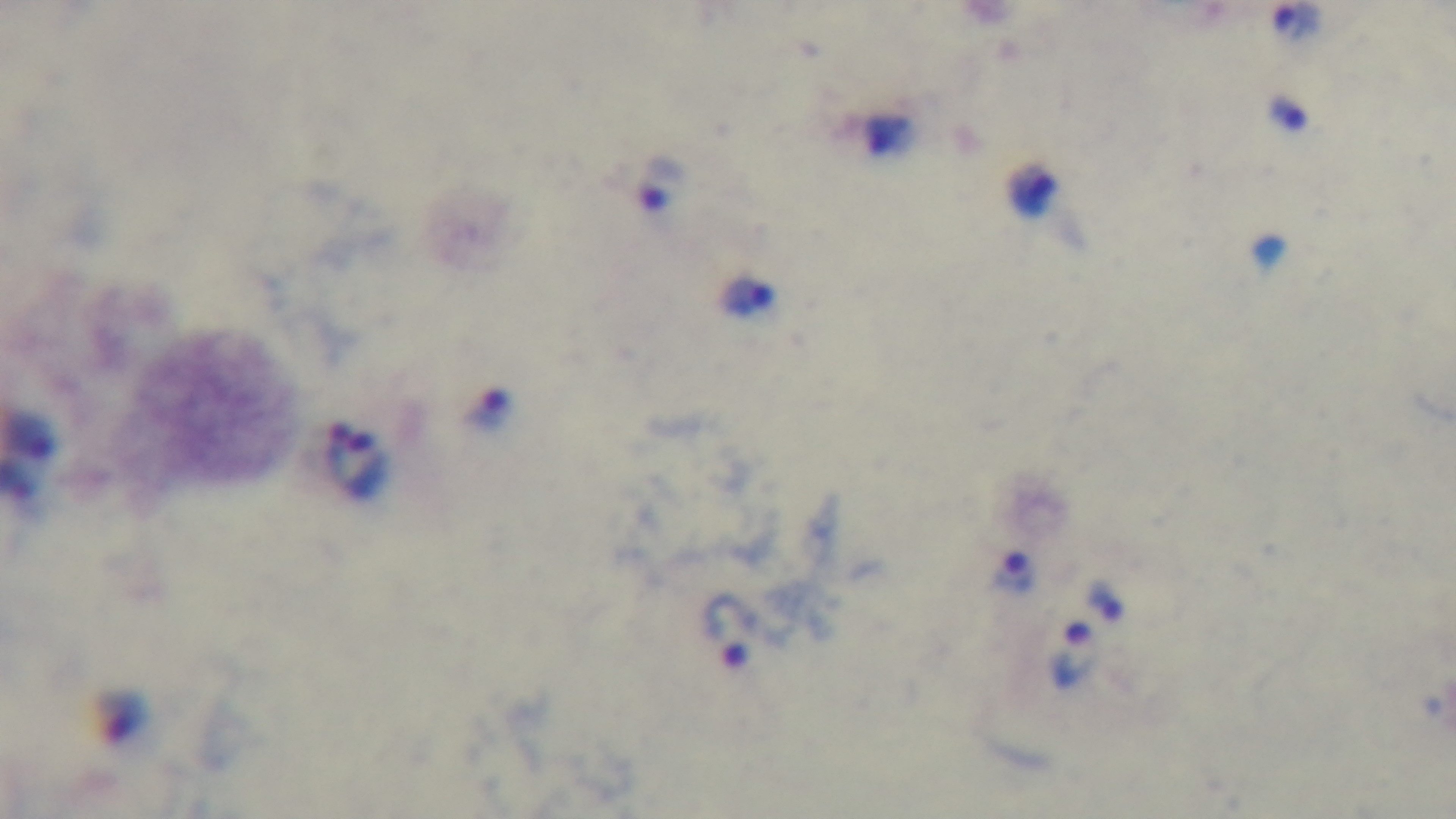

Captured with a mounted 4K digital camera. Giemsa-stained. Preparation: thick. One field from the slide. Malaria status: infected. Light microscopy. Oil-immersion objective, 100x.